Outline platelets.
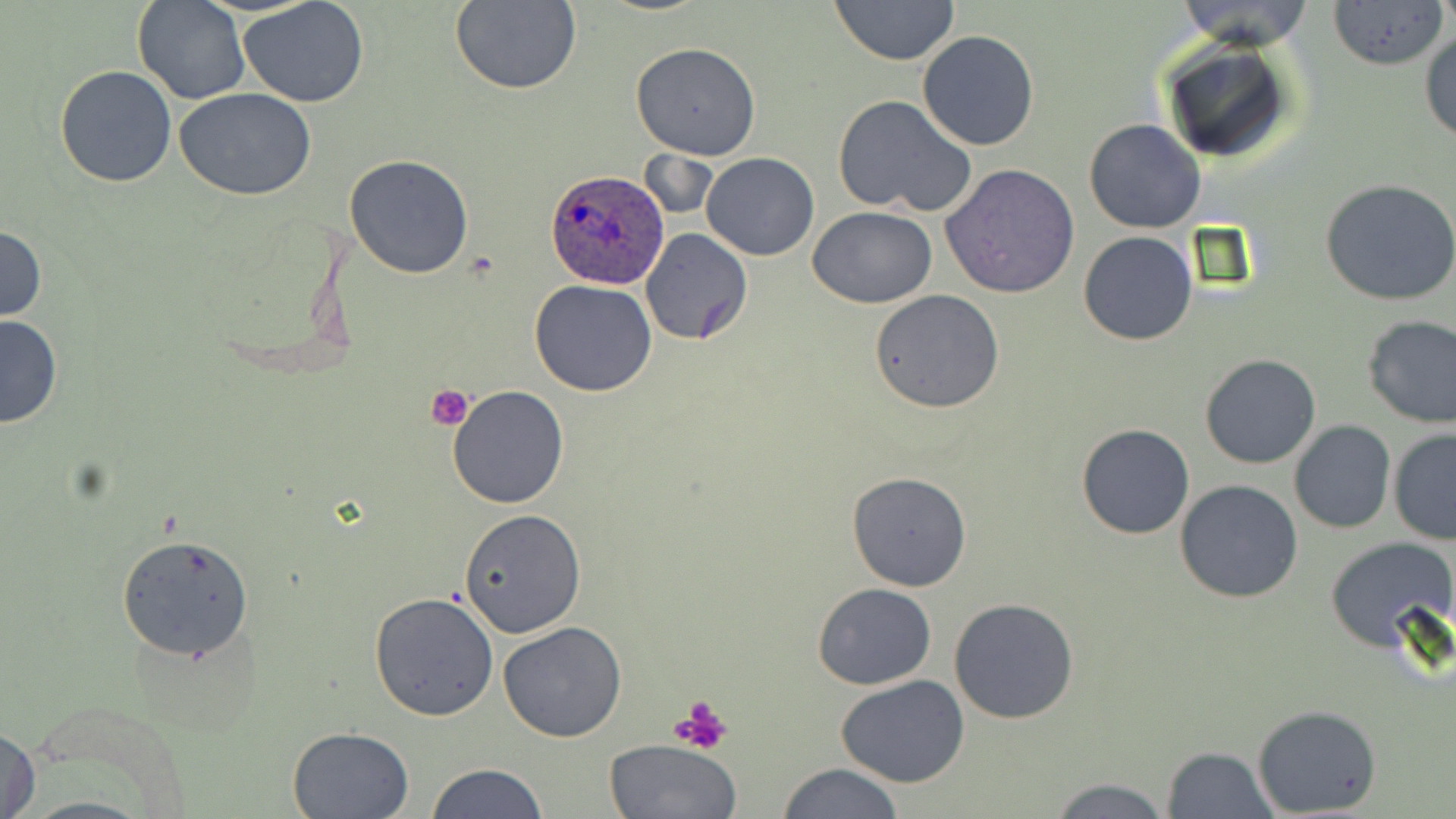

Approximate bounding boxes as [x1, y1, x2, y2] in pixels.
Platelets: [428, 383, 475, 428], [673, 696, 732, 752].

Plasmodium ovale-infected red blood cell locations: [546, 169, 671, 290]. Uninfected red blood cell locations: [134, 0, 250, 104], [239, 0, 368, 108], [829, 0, 959, 65], [449, 1, 581, 94], [1327, 1, 1448, 70], [141, 7, 363, 127], [1420, 28, 1456, 146], [917, 30, 1038, 151], [1156, 37, 1300, 167], [629, 42, 761, 160], [55, 64, 177, 186], [174, 88, 316, 201], [832, 93, 977, 217], [1084, 119, 1206, 234], [638, 150, 718, 222], [701, 152, 819, 259], [345, 154, 473, 278], [941, 165, 1081, 299], [1320, 178, 1456, 305], [807, 207, 937, 308], [0, 224, 46, 323], [640, 230, 751, 345], [1078, 231, 1197, 345], [530, 280, 657, 398], [868, 289, 1004, 414], [0, 313, 62, 429], [1360, 316, 1456, 428], [1199, 354, 1321, 470], [447, 384, 568, 508], [1289, 421, 1395, 534], [1077, 423, 1196, 540], [1388, 429, 1456, 546], [845, 471, 972, 593], [1174, 479, 1304, 603], [458, 509, 587, 638], [116, 534, 255, 659], [1324, 537, 1455, 652], [812, 582, 938, 690], [368, 591, 499, 722], [949, 596, 1079, 724], [499, 621, 626, 743], [834, 676, 970, 787], [1252, 704, 1381, 817], [287, 726, 415, 819], [1, 727, 41, 819], [604, 738, 740, 819], [1162, 745, 1279, 819], [422, 762, 546, 819], [776, 763, 906, 819], [1047, 776, 1174, 819]. Slide-level diagnosis: Plasmodium ovale. May-Grünwald-Giemsa stain. Image is 1456×819 pixels. 1000x magnification. Thin blood smear. One field of a larger specimen. Light microscopy.